Assess for parasitized red blood cells.
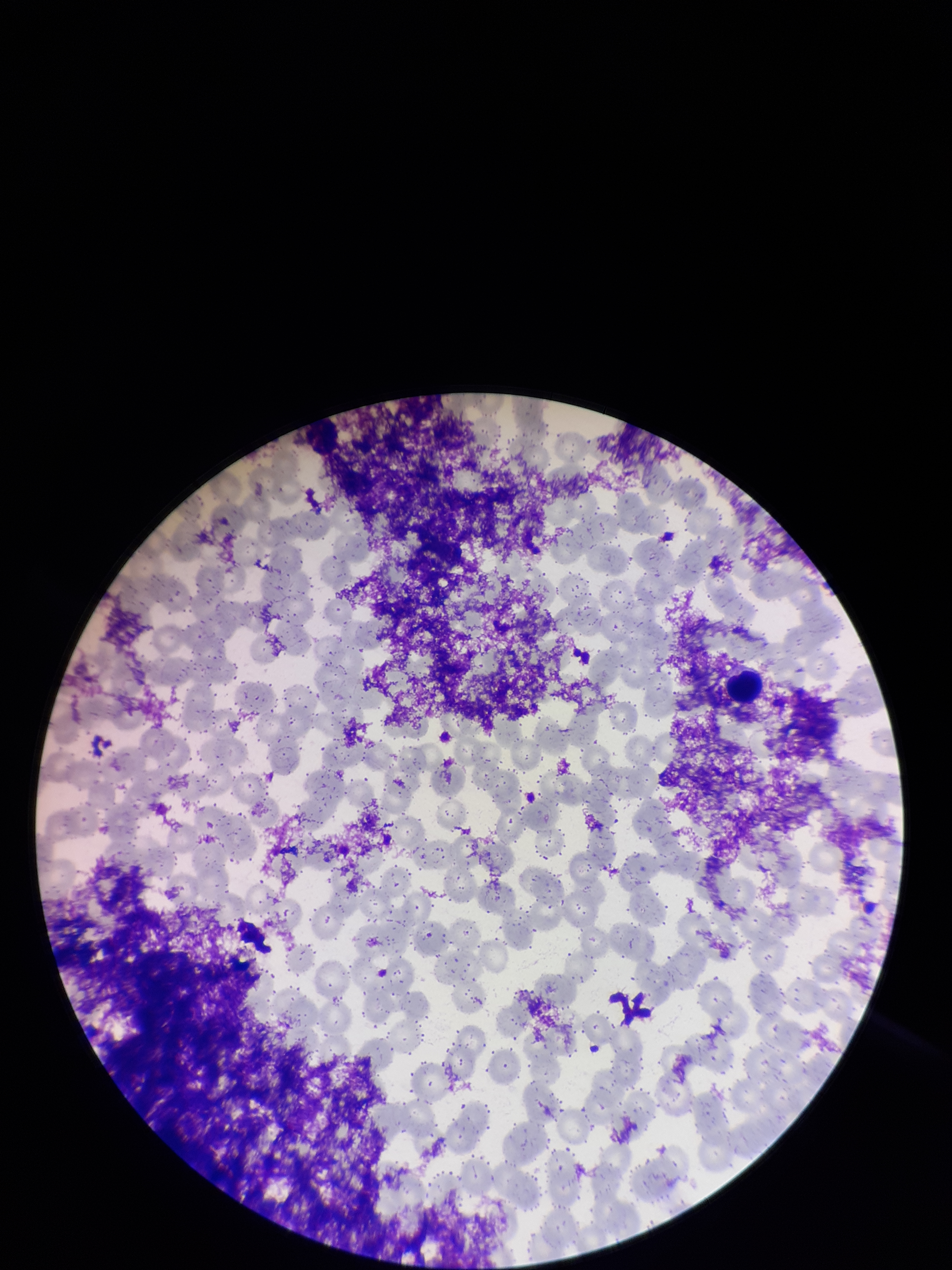
None detected.

{
  "red_blood_cell_count": 298,
  "field_of_view": "single",
  "patient_malaria_status": "negative",
  "stain": "Giemsa",
  "parasitized_red_blood_cell_count": 0,
  "preparation": "thin smear",
  "capture": "smartphone photograph through the microscope eyepiece",
  "image_size": "952×1270 pixels"
}